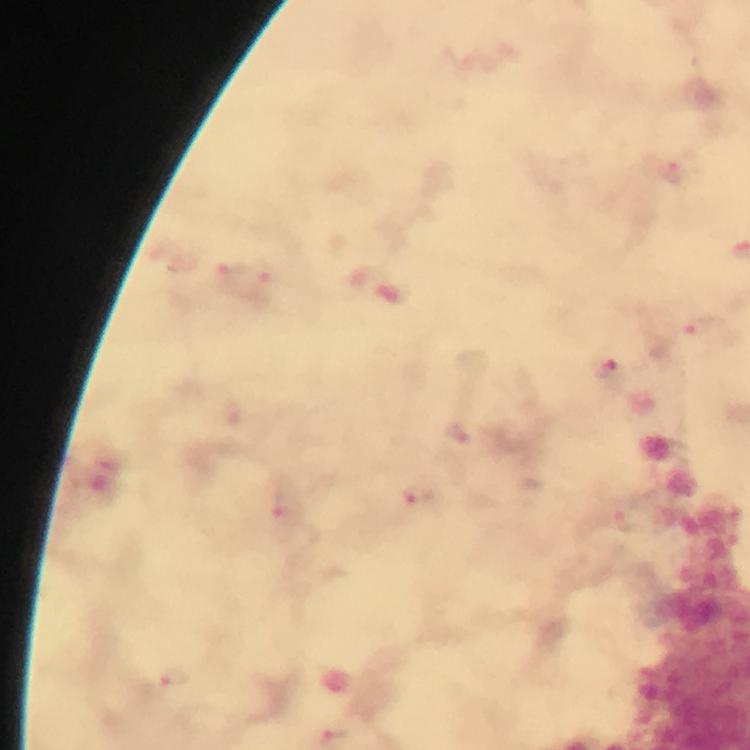

magnification = 100x
image size = 750×750 pixels
immersion oil = used
context = from a diagnostic examination for malaria
capture = smartphone camera through the microscope
Plasmodium parasite locations = approximate object centers, in pixels from the top-left corner: (x=677, y=172), (x=232, y=273), (x=268, y=273), (x=704, y=326), (x=608, y=373), (x=456, y=430), (x=420, y=499), (x=289, y=516), (x=173, y=678), (x=334, y=736)
cropped from = one field of view
stain = Giemsa
preparation = thick smear